Assess this cell for malaria.
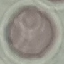
It is uninfected.

{
  "stain": "Giemsa",
  "image_type": "automatically extracted cell patch, resized to 64 × 64 pixels",
  "preparation": "thin smear",
  "capture": "smartphone camera at the microscope eyepiece"
}